Report the malaria status of this cell.
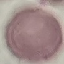

It is uninfected.

stain = Giemsa
preparation = thin blood film
capture = smartphone through the microscope eyepiece
image type = cell patch, automatically extracted from a larger field of view and resized to 64 × 64 pixels